Assess for Plasmodium parasites.
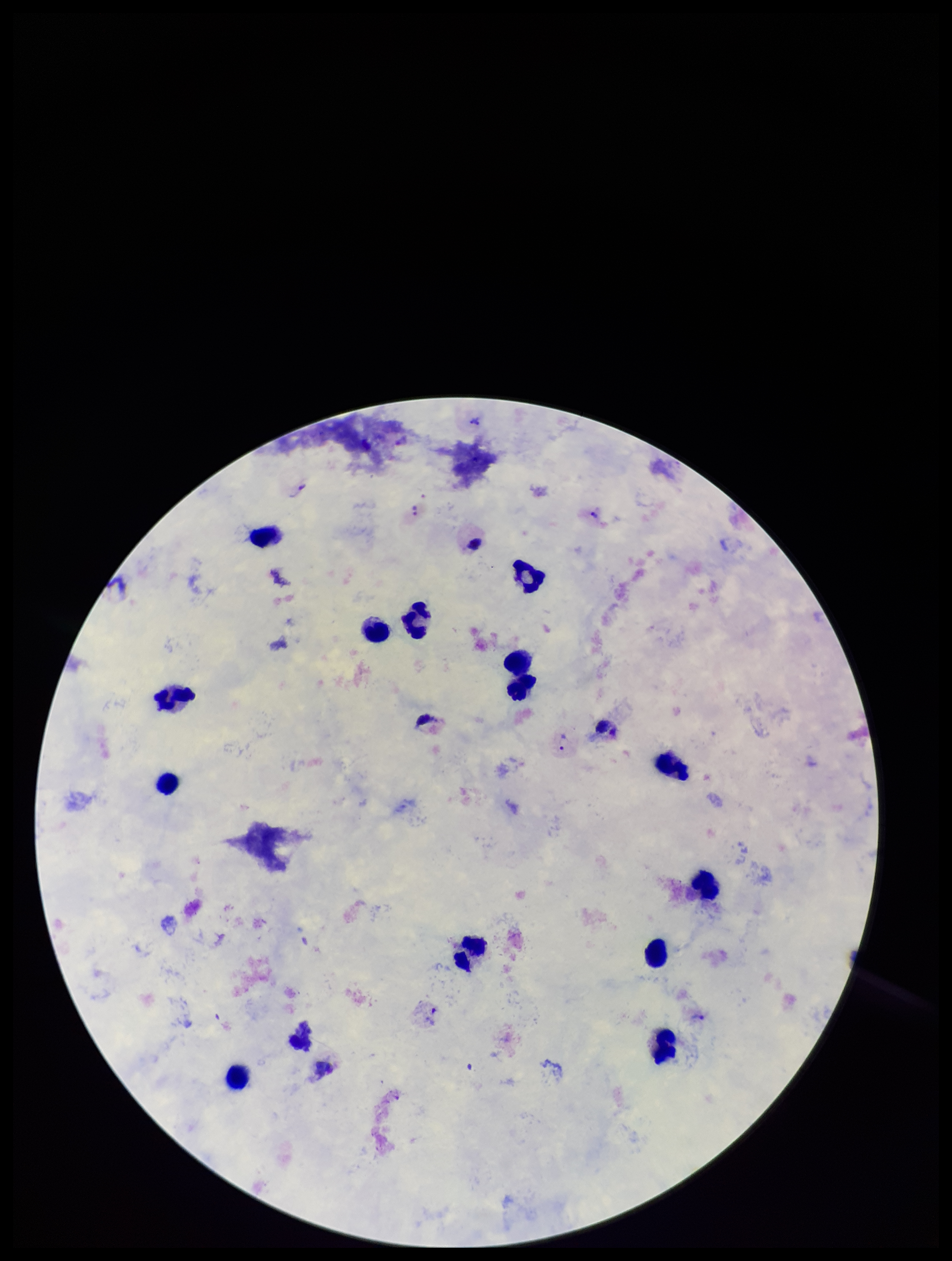

Seen.

Summary:
  - Preparation: thick smear
  - Parasite count: 4
  - Image size: 952×1261 pixels
  - Species reported for this patient: Plasmodium vivax
  - Capture: smartphone photograph through the microscope eyepiece
  - Field of view: single
  - Leukocyte count: 14
  - Patient malaria status: positive
  - Stain: Giemsa